Classify this cell by malaria status.
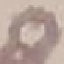
It is uninfected.

Summary:
  - Preparation: thin blood smear
  - Stain: Giemsa
  - Capture: smartphone through the microscope eyepiece
  - Image type: automatically extracted cell patch, resized to 64 × 64 pixels